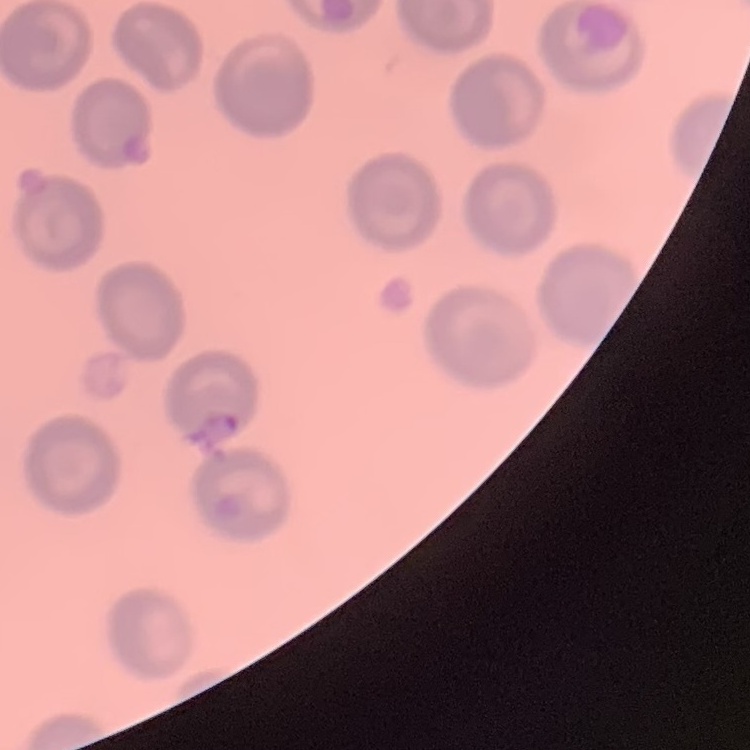 The erythrocytes show no rouleaux formation. Thin blood film. One tile cut from a larger photomicrograph. Stained with either Field's or Giemsa.